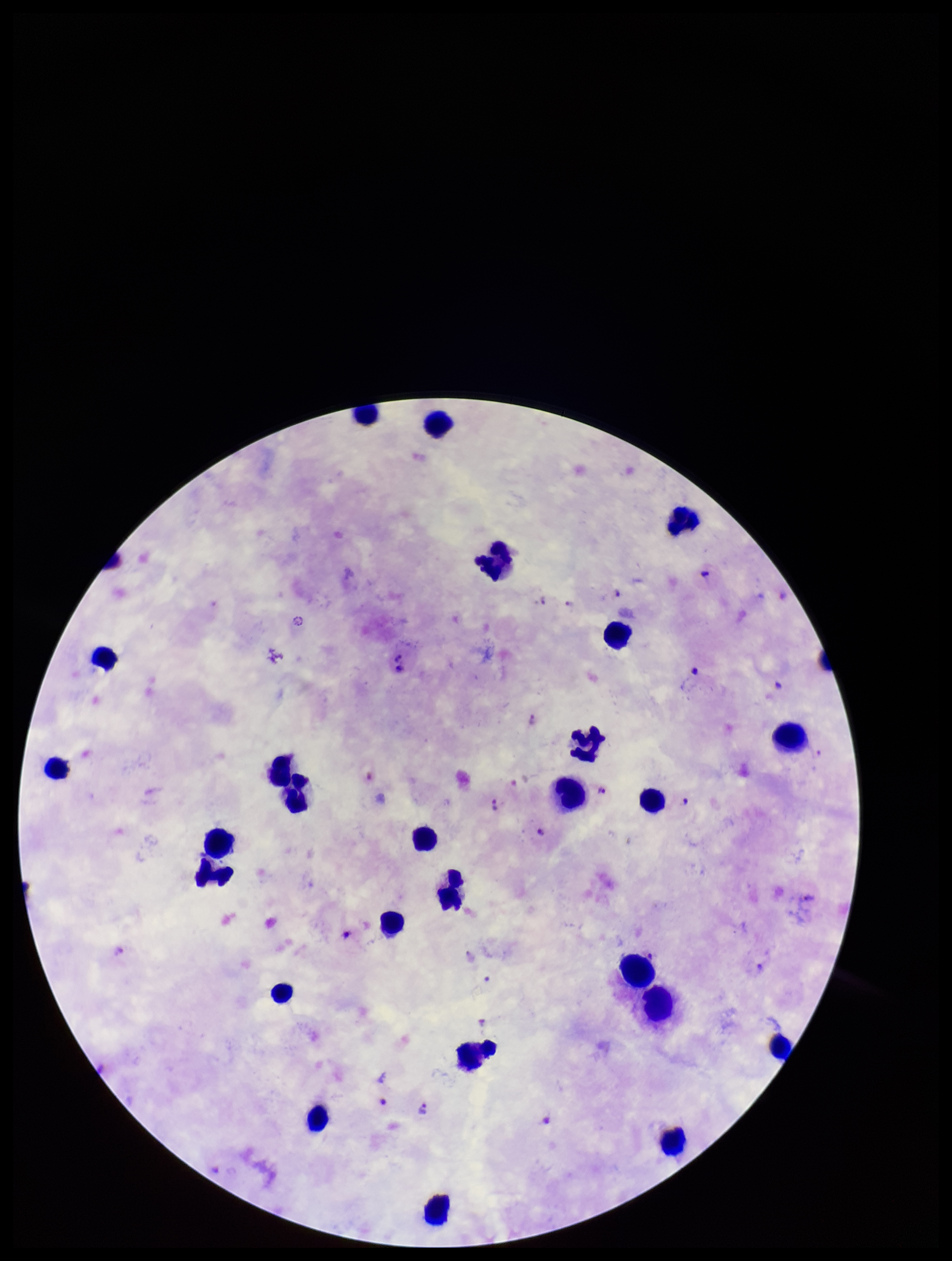
capture: smartphone photograph through the microscope eyepiece
image_size: 952×1261 pixels
species_reported_for_this_patient: Plasmodium falciparum
leukocyte_count: 26
plasmodium_parasites: detected
parasite_count: 9
preparation: thick smear
field_of_view: one from this slide
stain: Giemsa
patient_malaria_status: infected